State which parasite is depicted.
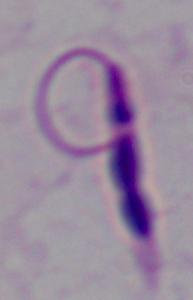
Leishmania.

Summary:
  - Magnification: 1000x
  - Modality: photomicrograph